State the blood parasite species.
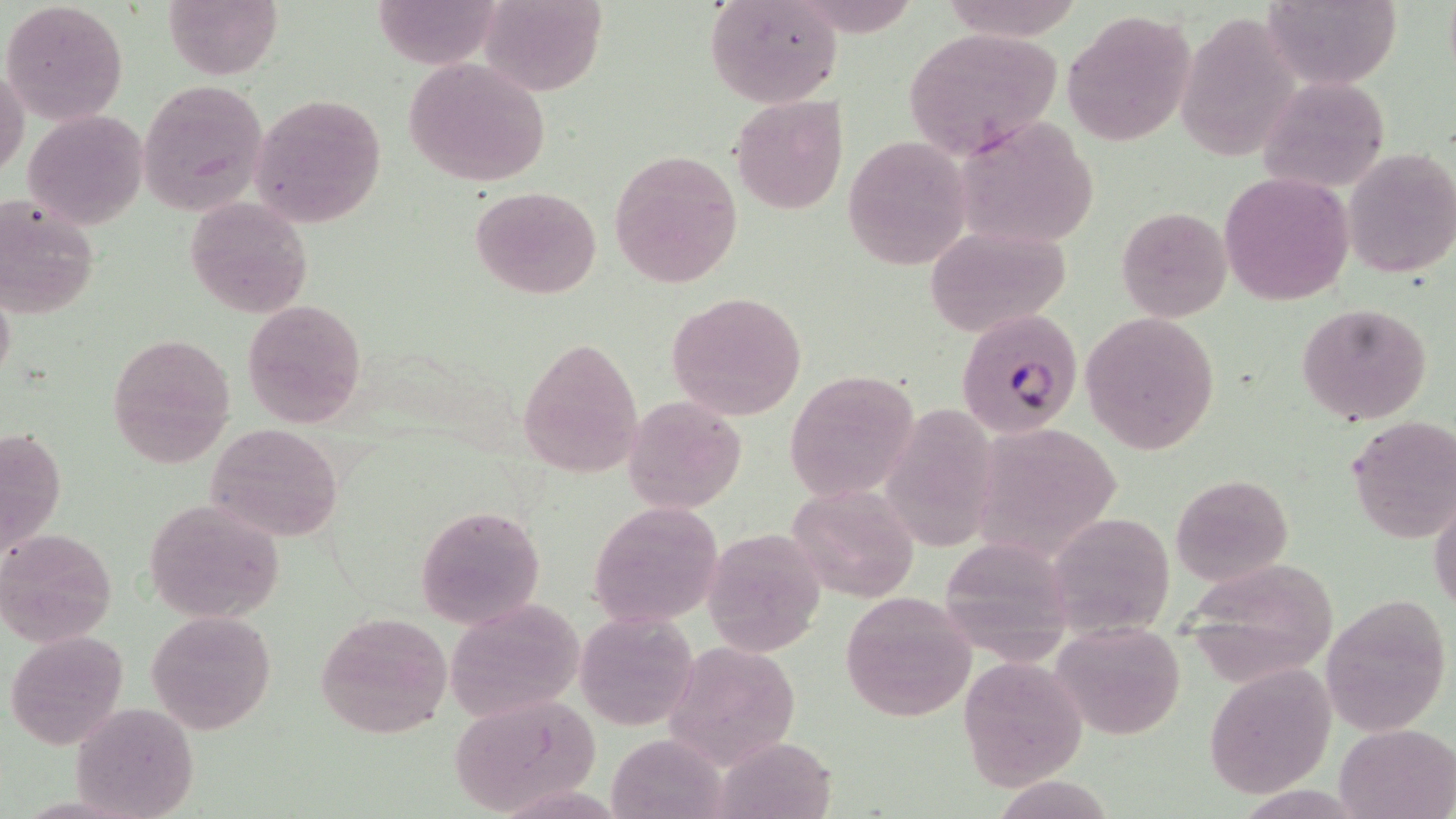
Plasmodium falciparum.

Summary:
  - Coordinate format: approximate bounding boxes as (x1, y1, x2, y2) in pixels
  - Uninfected red blood cell locations: (2, 0, 128, 124), (163, 0, 282, 79), (371, 0, 501, 69), (478, 0, 605, 96), (705, 0, 842, 108), (937, 0, 1081, 40), (1262, 0, 1401, 89), (1062, 10, 1196, 146), (1176, 13, 1298, 158), (902, 26, 1065, 159), (403, 56, 553, 188), (1, 65, 28, 181), (1256, 74, 1391, 194), (138, 78, 271, 218), (248, 94, 386, 226), (732, 94, 849, 214), (22, 108, 148, 230), (956, 116, 1102, 247), (842, 137, 971, 269), (609, 148, 744, 290), (1342, 148, 1455, 280), (1218, 172, 1354, 305), (470, 187, 603, 298), (0, 193, 101, 320), (184, 197, 313, 319), (1116, 205, 1233, 321), (923, 223, 1071, 338), (0, 281, 15, 391), (666, 291, 807, 422), (243, 299, 366, 428), (1296, 302, 1433, 425), (1080, 310, 1222, 455), (105, 333, 235, 466), (517, 338, 643, 477), (785, 368, 919, 504), (622, 397, 746, 513), (883, 401, 998, 547), (1346, 415, 1456, 543), (2, 423, 67, 560), (205, 423, 344, 543), (984, 425, 1123, 559), (1170, 474, 1293, 584), (789, 485, 921, 602), (1430, 492, 1455, 619), (143, 500, 283, 622), (589, 501, 724, 630), (418, 505, 543, 629), (1066, 509, 1185, 649), (2, 526, 117, 645), (699, 529, 829, 658), (934, 537, 1077, 664), (1182, 560, 1343, 682), (839, 590, 977, 722), (1323, 596, 1453, 733), (447, 602, 585, 721), (316, 609, 453, 739), (575, 610, 696, 731), (146, 611, 276, 733), (1050, 621, 1187, 740), (4, 630, 129, 750), (664, 639, 803, 771), (957, 655, 1087, 791), (1203, 666, 1336, 800), (445, 693, 602, 815), (70, 701, 200, 818), (1334, 722, 1456, 818), (605, 733, 731, 819), (710, 735, 839, 819)
  - Plasmodium falciparum-infected red blood cell locations: (961, 308, 1087, 441)
  - Preparation: thin blood smear
  - Magnification: 1000x
  - Field of view: single
  - Image size: 1456×819 pixels
  - Stain: May-Grünwald-Giemsa
  - Modality: light microscopy